Classify this cell by malaria status.
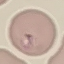

It is parasitized.

Summary:
  - Capture: smartphone camera at the microscope eyepiece
  - Stain: Giemsa
  - Preparation: thin blood smear
  - Image type: automatically extracted cell patch, resized to 64 × 64 pixels